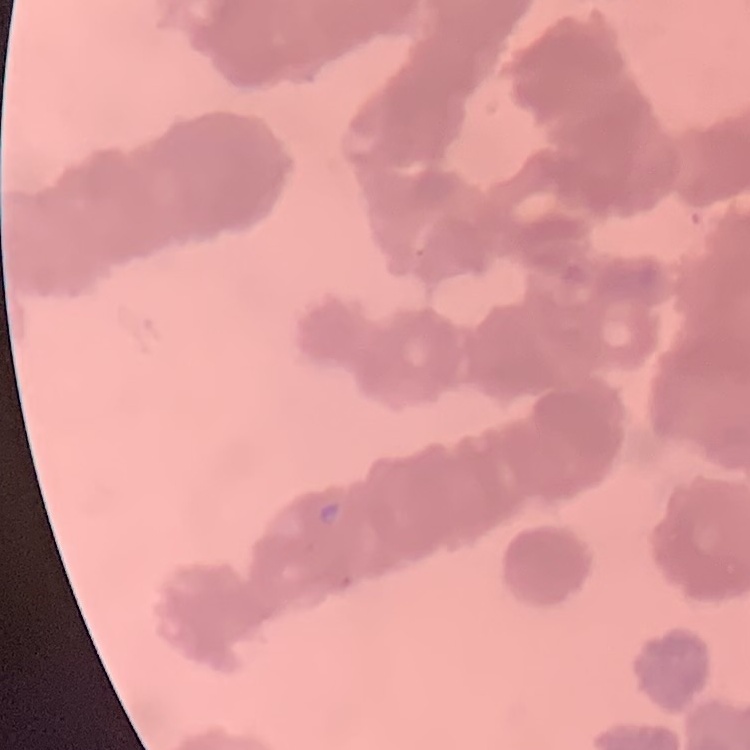
Summary:
  - Red blood cell morphology: rouleaux formation
  - Preparation: thin blood smear
  - Image type: square crop of a larger photomicrograph
  - Stain: Field's or Giemsa